Locate malaria parasites and leukocytes.
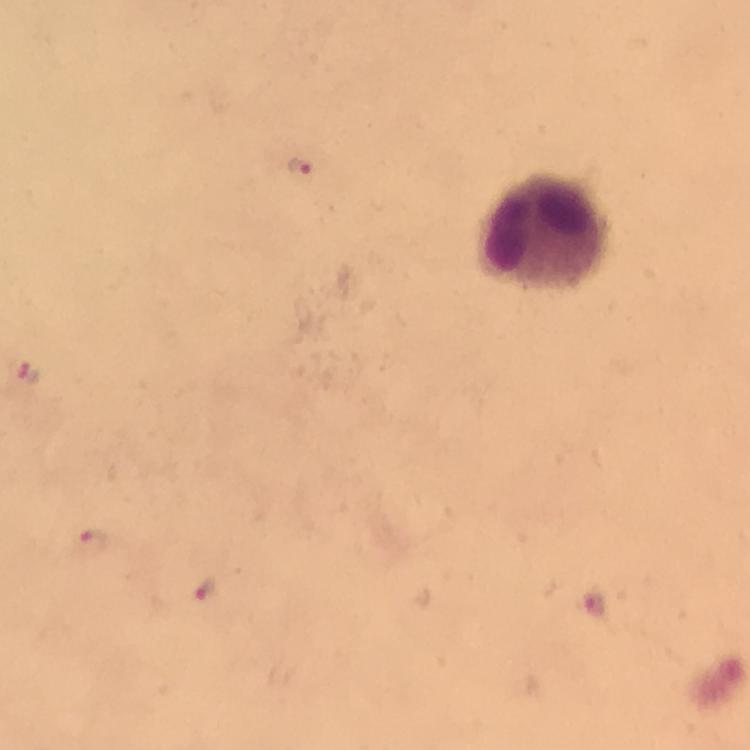

Approximate centers as {x, y} in pixels.
Malaria parasites: {303, 172}, {29, 373}, {93, 542}, {206, 591}, {594, 606}.
Leukocytes: {545, 233}.

preparation = thick blood film
cropped from = one field of view
context = from a diagnostic examination for malaria
capture = smartphone camera through the microscope
immersion oil = used
image size = 750×750 pixels
stain = Giemsa
magnification = 100x